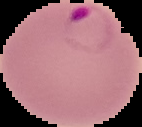
Summary:
  - Image type: cell region segmented out of the field of view; surrounding area masked to black
  - Preparation: thin blood film
  - Image size: 142×127 pixels
  - Malaria status: parasitized